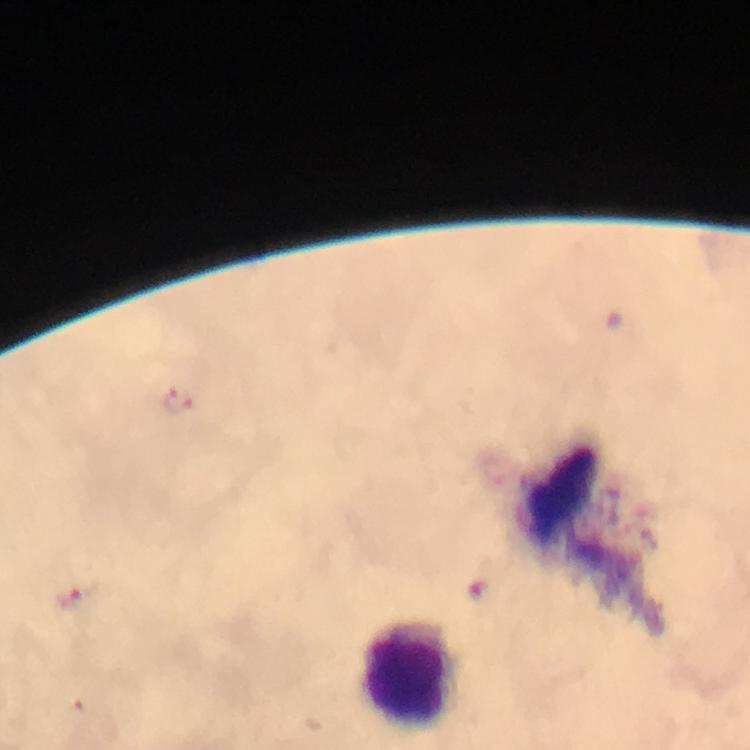

Approximate centers as {x, y} in pixels.
Summary:
  - Leukocyte locations: {410, 672}
  - Malaria parasite locations: {178, 400}, {71, 600}
  - Magnification: 100x
  - Stain: Giemsa
  - Preparation: thick blood smear
  - Image size: 750×750 pixels
  - Context: from a diagnostic examination for malaria
  - Capture: smartphone mounted on the microscope
  - Immersion oil: used
  - Cropped from: a single field of view